Assess the morphology of the red blood cells.
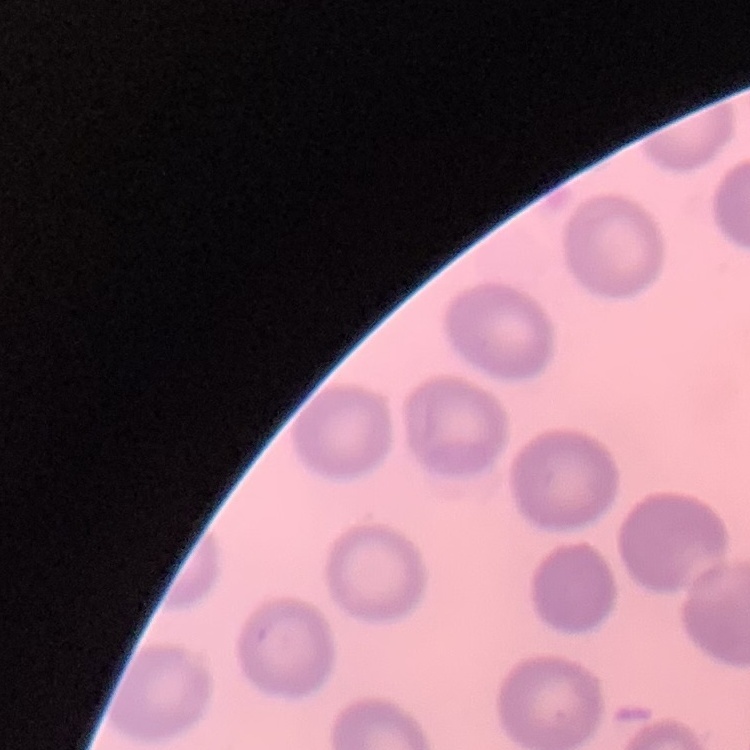

No rouleaux formation.

Summary:
  - Preparation: thin blood film
  - Stain: Field's or Giemsa
  - Image type: square crop of a larger photomicrograph